Report the malaria status of this cell.
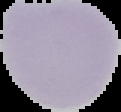
Uninfected.

preparation = thin blood film
image type = cell region segmented out of the field of view; surrounding area masked to black
image size = 121×112 pixels